State which parasite is depicted.
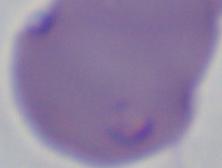
Babesia.

Micrograph. 1000x magnification.